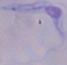
Summary:
  - Magnification: 1000x
  - Modality: photomicrograph
  - Identification: trypanosome